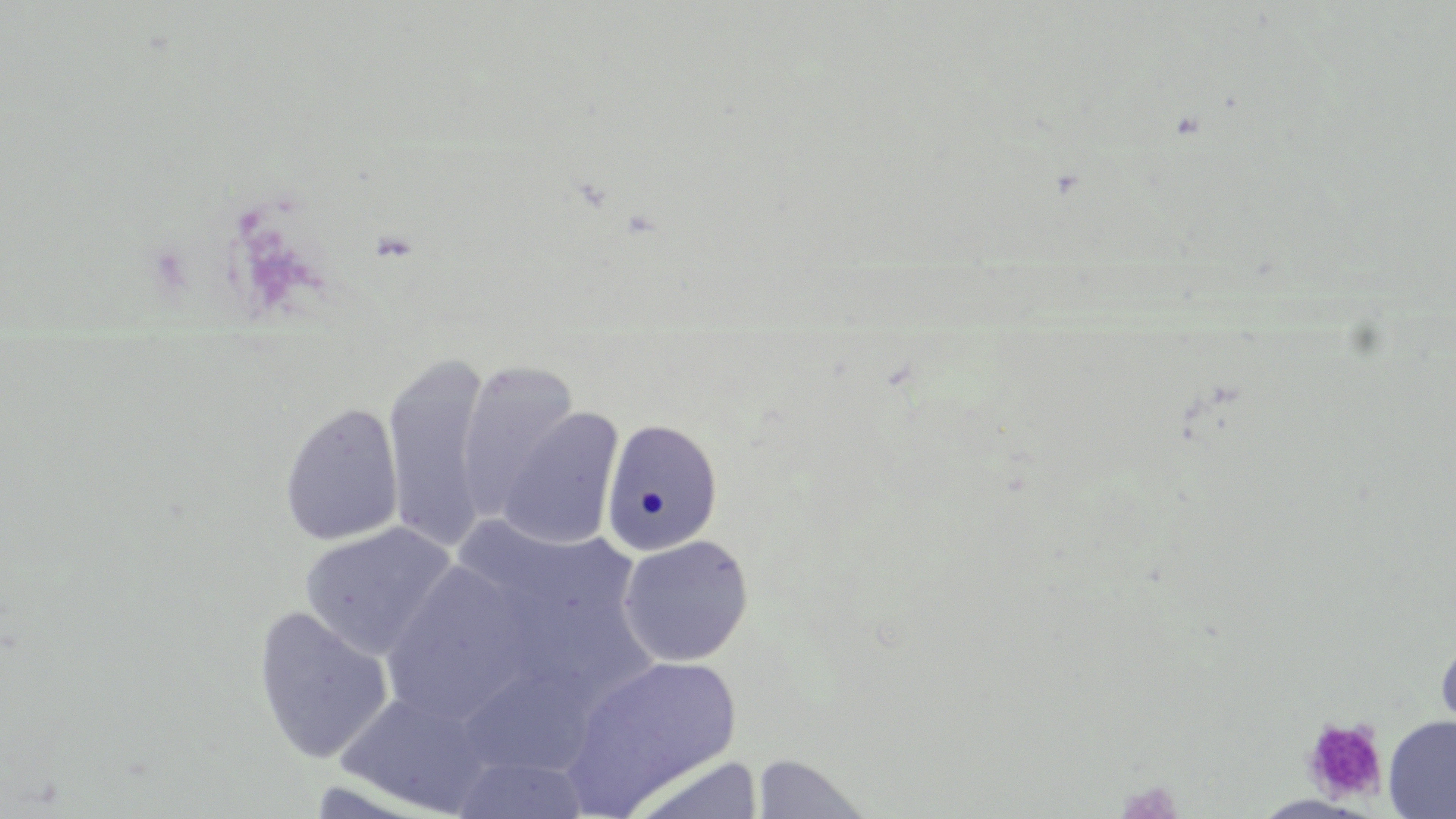
{
  "slide_level_diagnosis": "no evidence of blood parasites",
  "field_of_view": "single",
  "modality": "light microscopy",
  "uninfected_red_blood_cell_locations": "approximate bounding boxes as (x1,y1)-(x2,y2) corner pairs in pixels: (381,354)-(495,555), (457,360)-(581,522), (278,401)-(404,546), (495,408)-(624,550), (600,418)-(724,556), (448,514)-(653,690), (299,522)-(458,661), (617,534)-(754,667), (381,561)-(535,724), (252,605)-(394,765), (1434,634)-(1456,742), (561,655)-(743,813), (334,687)-(496,816), (1382,715)-(1456,818), (749,753)-(874,818), (450,754)-(593,817), (624,755)-(766,819), (1251,794)-(1375,818)",
  "platelet_locations": "approximate bounding boxes as (x1,y1)-(x2,y2) corner pairs in pixels: (1302,717)-(1388,805)",
  "preparation": "thin blood film",
  "image_size": "1456×819 pixels",
  "magnification": "1000x",
  "stain": "May-Grünwald-Giemsa"
}